Assess this cell for malaria.
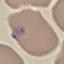

Parasitized.

{
  "stain": "Giemsa",
  "capture": "smartphone camera at the microscope eyepiece",
  "image_type": "automatically extracted cell patch, resized to 64 × 64 pixels",
  "preparation": "thin blood film"
}